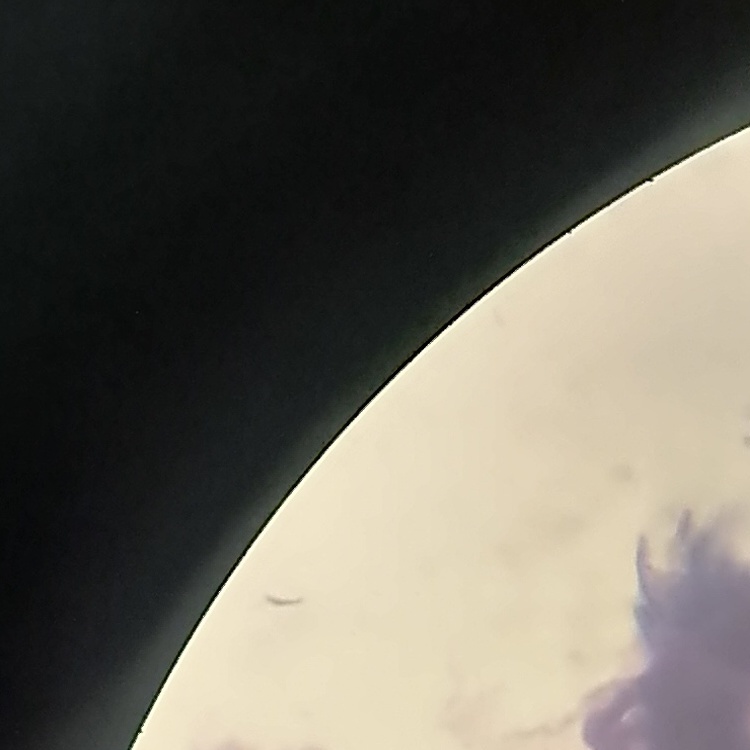

erythrocyte morphology = rouleaux formation
stain = Field's or Giemsa
image type = one tile cut from a larger photomicrograph
preparation = thin blood smear